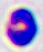

modality = micrograph
identification = leukocyte
magnification = 400x